Name the parasite shown.
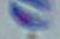
This is Toxoplasma gondii.

magnification = 1000x
modality = micrograph